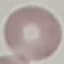
Summary:
  - Malaria status: uninfected
  - Capture: smartphone through the microscope eyepiece
  - Preparation: thin blood film
  - Image type: cell patch, automatically extracted from a larger field of view and resized to 64 × 64 pixels
  - Stain: Giemsa